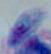 Photomicrograph. 1000x magnification. Toxoplasma gondii is shown.